Point out each malaria parasite.
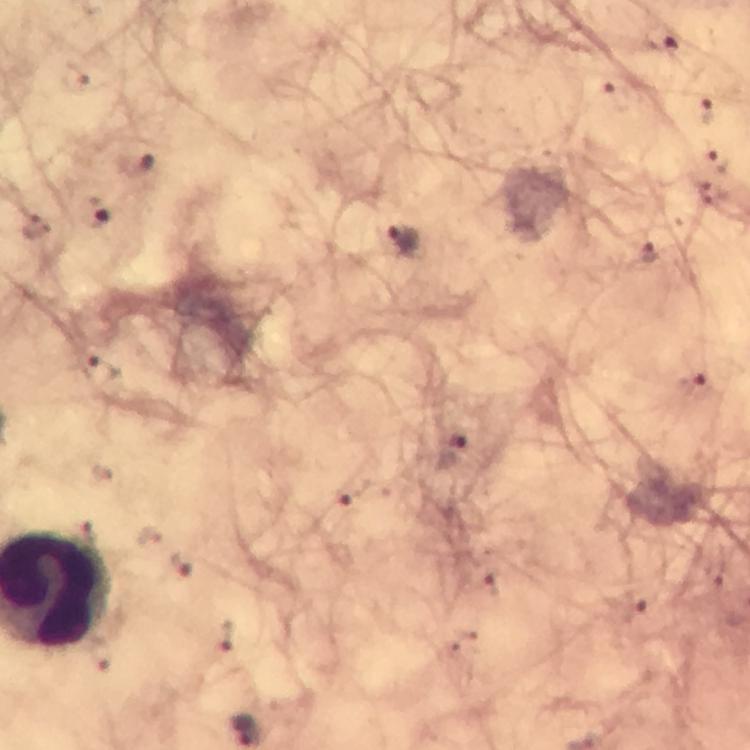

Approximate centers as [x, y] in pixels.
Malaria parasites: [660, 37], [618, 96], [707, 109], [717, 160], [712, 194], [97, 212], [403, 240], [648, 253], [693, 385], [451, 449], [346, 494], [182, 565].

preparation = thick blood film
image size = 750×750 pixels
stain = Giemsa
immersion oil = used
capture = smartphone mounted on the microscope
magnification = 100x
cropped from = a single field of view
context = from a malaria diagnostic workup